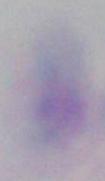

identification = Toxoplasma gondii
modality = photomicrograph
magnification = 1000x